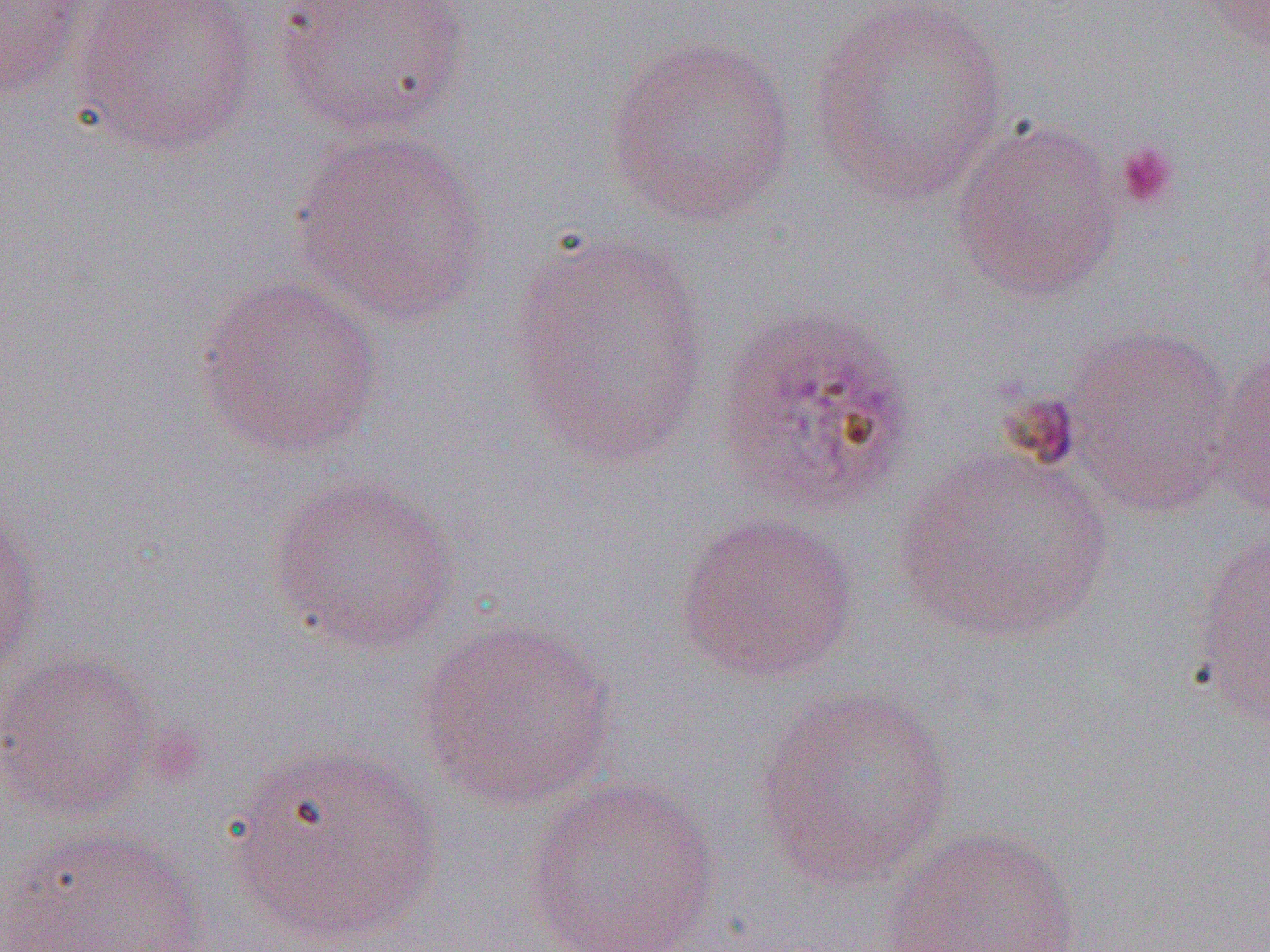

slide-level diagnosis = Plasmodium ovale
uninfected red blood cell locations = approximate bounding boxes as (x1, y1, x2, y2) in pixels: (0, 0, 89, 103), (73, 0, 263, 159), (271, 0, 472, 138), (805, 0, 1010, 208), (1192, 0, 1269, 50), (604, 34, 800, 229), (949, 117, 1124, 303), (289, 129, 492, 327), (504, 232, 715, 470), (194, 274, 384, 460), (1061, 323, 1237, 516), (1207, 338, 1270, 515), (893, 447, 1116, 645), (267, 472, 462, 656), (0, 504, 43, 689), (674, 511, 859, 684), (1190, 528, 1270, 725), (414, 616, 618, 811), (0, 648, 157, 822), (751, 684, 957, 890), (227, 742, 444, 946), (524, 775, 722, 952), (880, 826, 1084, 952), (3, 828, 211, 951)
modality = light microscopy
platelet locations = approximate bounding boxes as (x1, y1, x2, y2) in pixels: (1114, 140, 1181, 210)
magnification = 1000x
field of view = single
Plasmodium ovale-infected red blood cell locations = approximate bounding boxes as (x1, y1, x2, y2) in pixels: (714, 303, 918, 516)
image size = 1270×952 pixels
preparation = thin blood film